Classify this cell by malaria status.
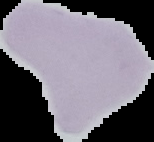

It is uninfected.

Image is 154×142 pixels. From a thin blood smear. Segmented cell region on a black background.